Name the parasite shown.
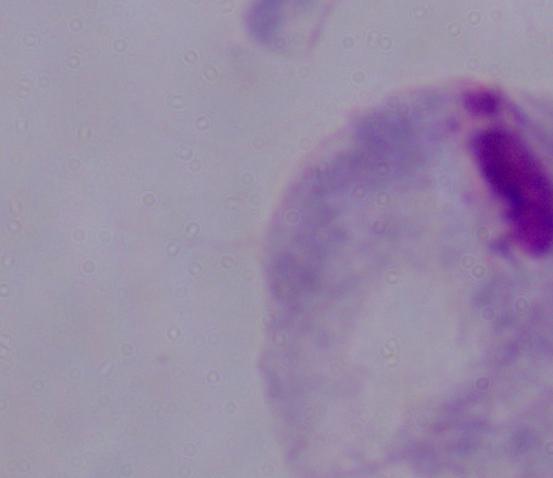
This is a trichomonad.

{
  "modality": "photomicrograph",
  "magnification": "1000x"
}